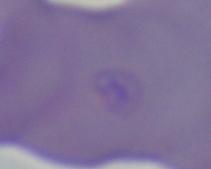
A Babesia parasite is shown. 1000x magnification. Photomicrograph.